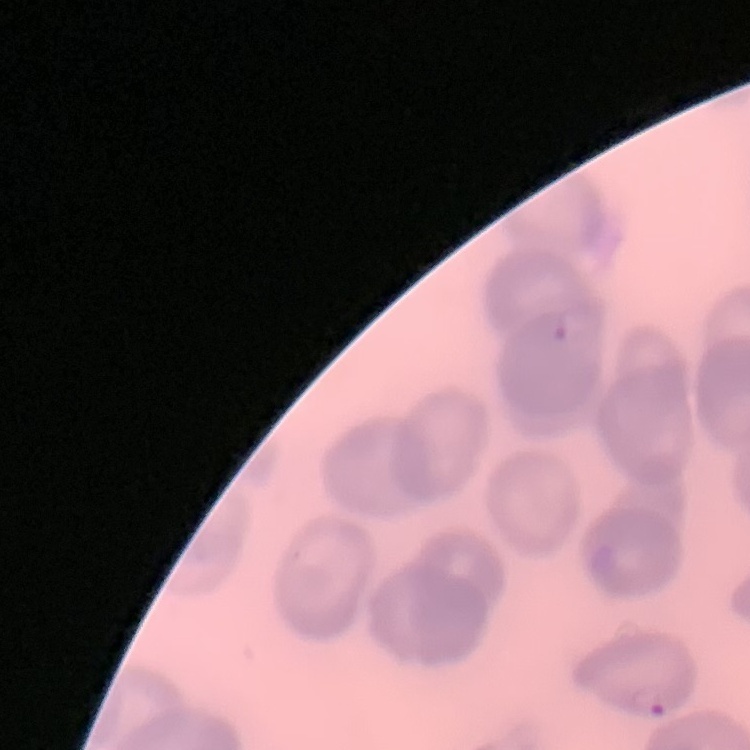
{
  "red_blood_cell_morphology": "no rouleaux formation",
  "stain": "Field's or Giemsa",
  "preparation": "thin peripheral smear",
  "image_type": "one tile cut from a larger photomicrograph"
}